Locate and identify every blood parasite.
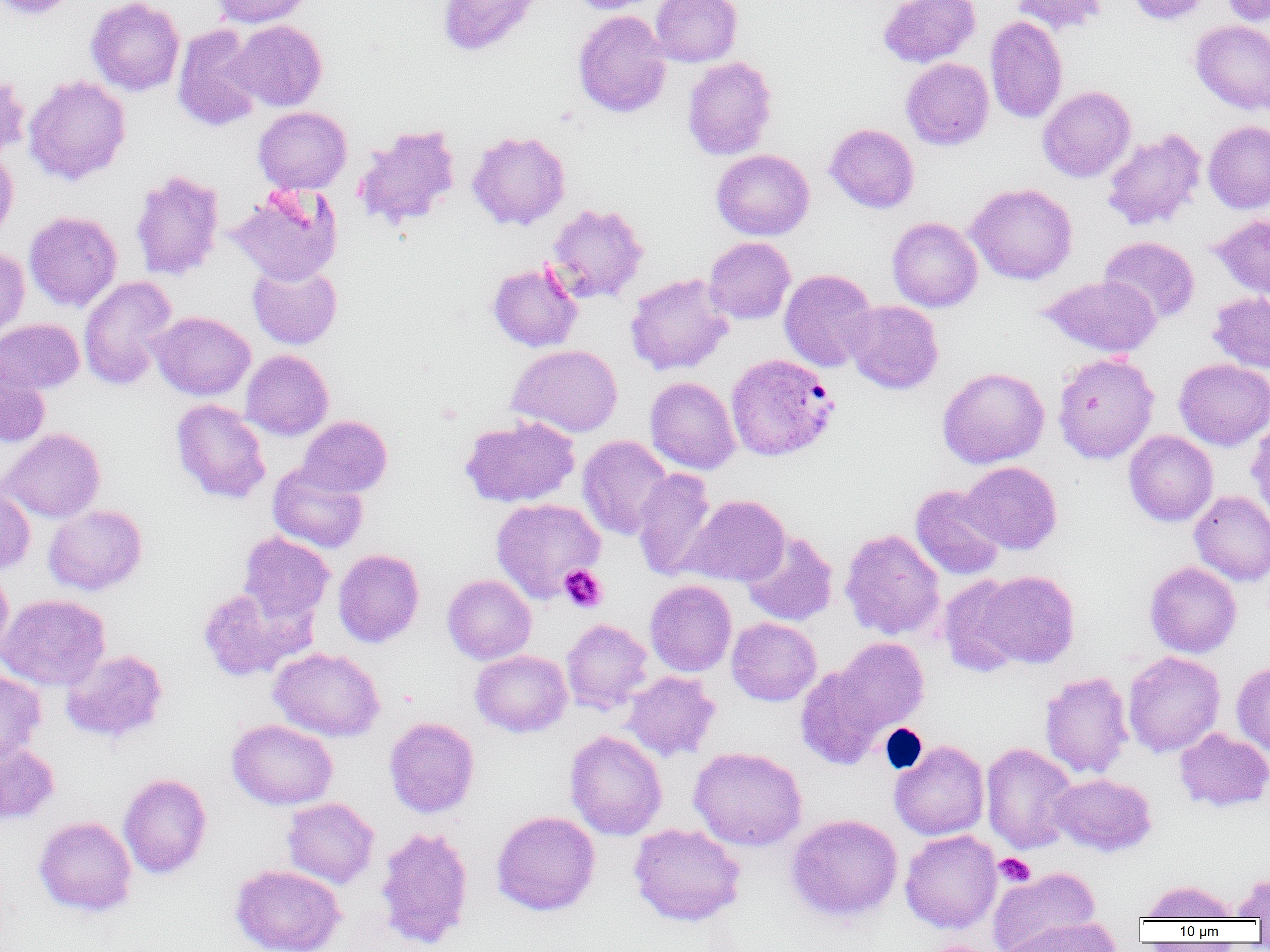
Approximate bounding boxes as (x1, y1, x2, y2) in pixels.
Plasmodium vivax-infected red blood cells: (725, 353, 838, 462).
No Plasmodium falciparum, Plasmodium ovale, Plasmodium malariae, Babesia divergens, or Trypanosoma brucei observed.

Platelet locations: (559, 565, 607, 613), (994, 853, 1035, 886). Uninfected red blood cell locations: (0, 0, 79, 19), (86, 0, 185, 96), (210, 0, 313, 28), (437, 0, 542, 56), (566, 0, 663, 14), (650, 0, 742, 67), (878, 0, 980, 68), (1010, 0, 1109, 35), (1127, 0, 1214, 25), (1221, 0, 1270, 26), (573, 10, 672, 118), (985, 15, 1068, 123), (229, 20, 327, 111), (1190, 20, 1270, 114), (173, 25, 265, 131), (681, 57, 777, 160), (901, 57, 994, 150), (0, 70, 30, 163), (24, 75, 131, 185), (1037, 86, 1136, 182), (253, 106, 352, 194), (1202, 120, 1270, 214), (825, 123, 919, 213), (353, 124, 461, 230), (1102, 128, 1206, 231), (467, 130, 571, 231), (0, 149, 18, 245), (711, 149, 814, 240), (130, 170, 225, 281), (966, 183, 1078, 285), (229, 184, 343, 286), (545, 203, 648, 304), (24, 211, 122, 311), (1211, 213, 1270, 301), (887, 217, 982, 312), (704, 236, 796, 324), (1099, 236, 1200, 325), (0, 246, 30, 343), (487, 261, 583, 352), (248, 262, 342, 349), (779, 269, 878, 372), (625, 273, 734, 376), (1039, 275, 1161, 358), (78, 276, 178, 390), (1208, 291, 1270, 374), (844, 300, 943, 394), (151, 311, 255, 401), (0, 318, 84, 397), (508, 344, 623, 438), (241, 350, 333, 440), (1053, 352, 1159, 464), (1174, 358, 1270, 451), (0, 359, 51, 448), (938, 366, 1050, 469), (645, 376, 741, 474), (171, 398, 270, 504), (297, 416, 392, 497), (460, 416, 580, 508), (1247, 419, 1270, 520), (1, 428, 105, 523), (1124, 430, 1218, 526), (578, 435, 673, 540), (960, 461, 1062, 554), (268, 464, 368, 553), (632, 468, 719, 580), (0, 484, 36, 576), (911, 485, 1006, 580), (1189, 491, 1270, 585), (682, 494, 790, 586), (491, 498, 605, 603), (44, 504, 147, 596), (840, 528, 945, 640), (741, 530, 839, 626), (238, 532, 335, 624), (333, 548, 424, 648), (1145, 561, 1242, 658), (0, 566, 13, 659), (974, 570, 1080, 669), (442, 574, 536, 664), (938, 574, 1029, 677), (645, 580, 737, 676), (197, 586, 306, 681), (0, 594, 110, 690), (726, 617, 822, 706), (561, 618, 653, 714), (833, 637, 929, 734), (269, 647, 385, 742), (61, 649, 167, 743), (470, 649, 572, 737), (1122, 651, 1225, 757), (1232, 661, 1270, 757), (796, 665, 890, 770), (0, 671, 46, 764), (622, 671, 720, 762), (1039, 671, 1134, 779), (384, 717, 480, 818), (227, 719, 337, 809), (1174, 728, 1270, 812), (565, 730, 667, 840), (0, 740, 59, 824), (890, 740, 989, 841), (980, 742, 1078, 854), (688, 746, 807, 851), (118, 773, 212, 879), (1049, 773, 1157, 856), (282, 797, 379, 889), (491, 811, 601, 916), (785, 813, 903, 923), (34, 816, 137, 916), (628, 823, 745, 926), (374, 826, 475, 950), (900, 830, 1002, 933), (230, 864, 345, 952), (988, 866, 1100, 952), (1232, 872, 1270, 921), (1139, 879, 1238, 921), (997, 918, 1122, 951). Slide-level diagnosis: Plasmodium vivax. Image is 1270×952 pixels. Thin blood film. Single field of view. Captured at 1000x magnification. Optical microscopy.